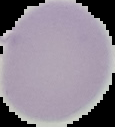
From a thin blood film. Image is 115×127 pixels. Segmented cell region on a black background. Malaria status: uninfected.